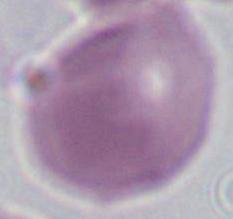

Captured at 1000x magnification. A red blood cell is seen. Micrograph.